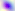
{
  "identification": "Toxoplasma gondii",
  "magnification": "400x",
  "modality": "micrograph"
}